Assess the morphology of the erythrocytes.
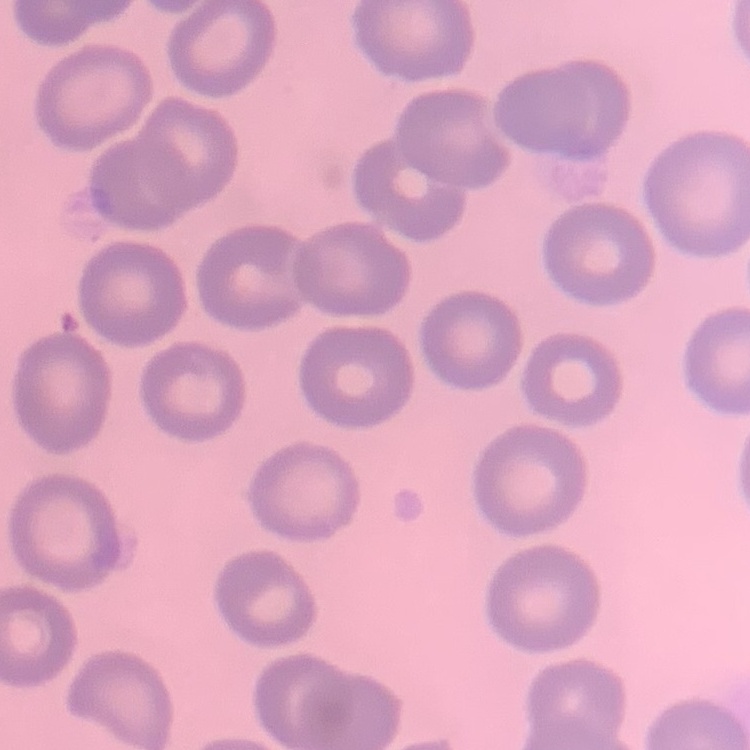
No rouleaux formation.

Stained with either Field's or Giemsa. Thin peripheral smear. One tile cut from a larger photomicrograph.